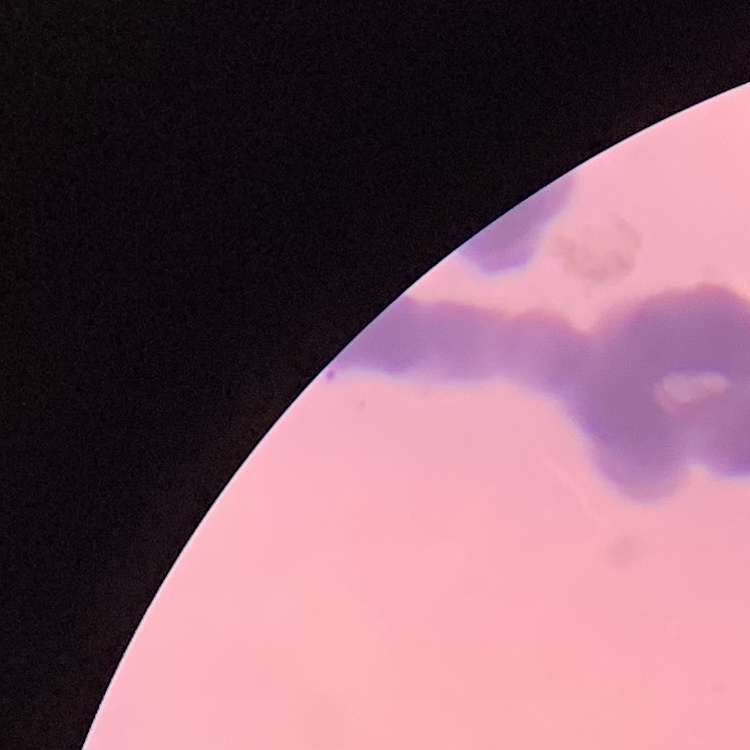
The erythrocytes exhibit rouleaux formation. Thin blood film. One tile cut from a larger photomicrograph. Field's or Giemsa stain.